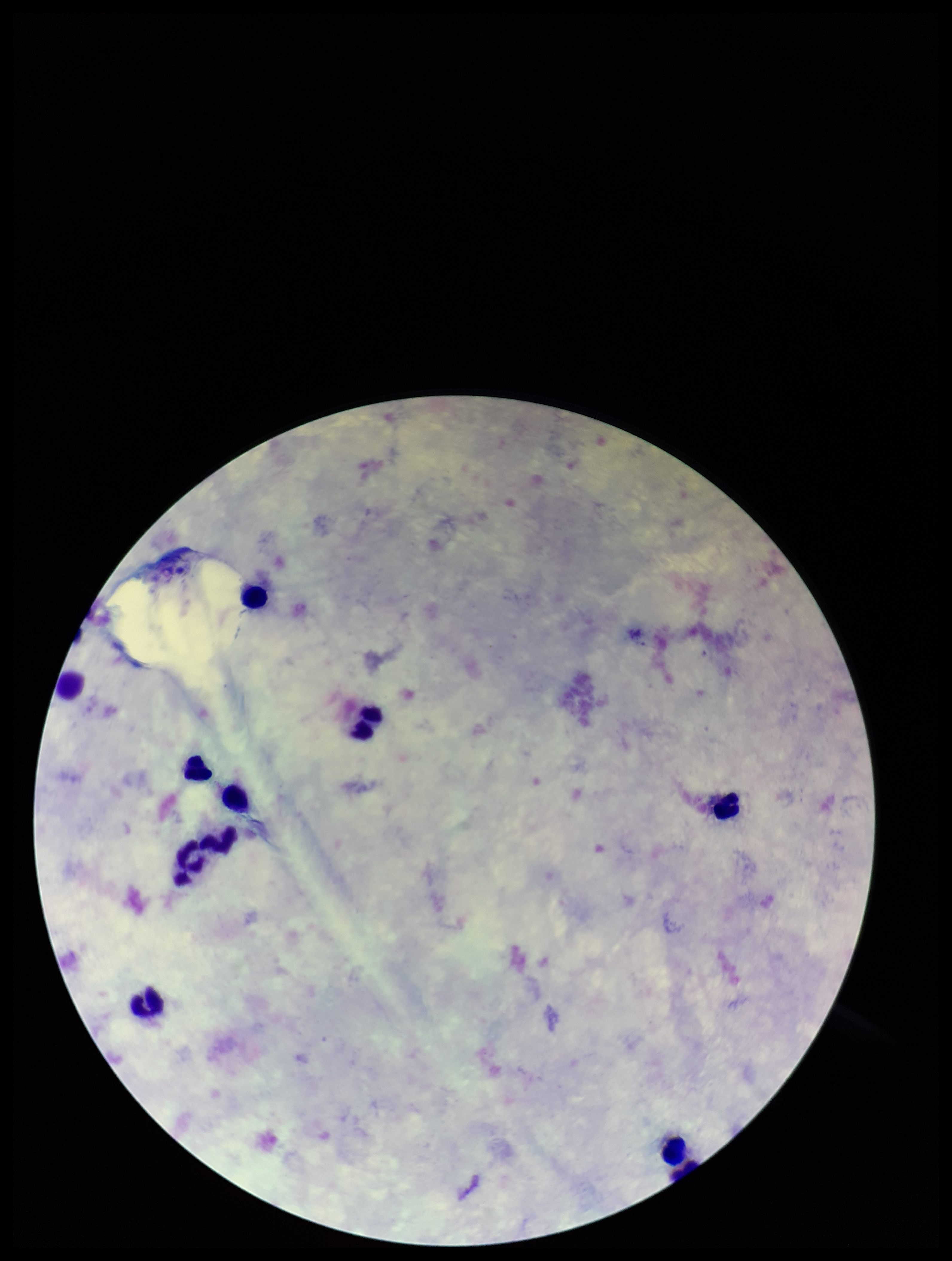
Image is 952×1261 pixels. Preparation: thick. Stained with Giemsa. Parasite count: 0. Patient malaria status: negative. Leukocyte count: 11. Photographed through the microscope eyepiece with a smartphone camera. Plasmodium parasites: none seen. Single field of view.